State which parasite is depicted.
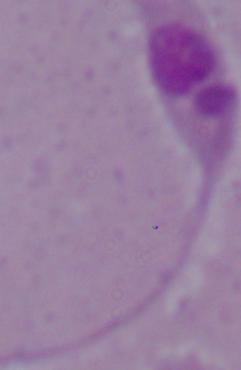
This is Leishmania.

Summary:
  - Modality: photomicrograph
  - Magnification: 1000x